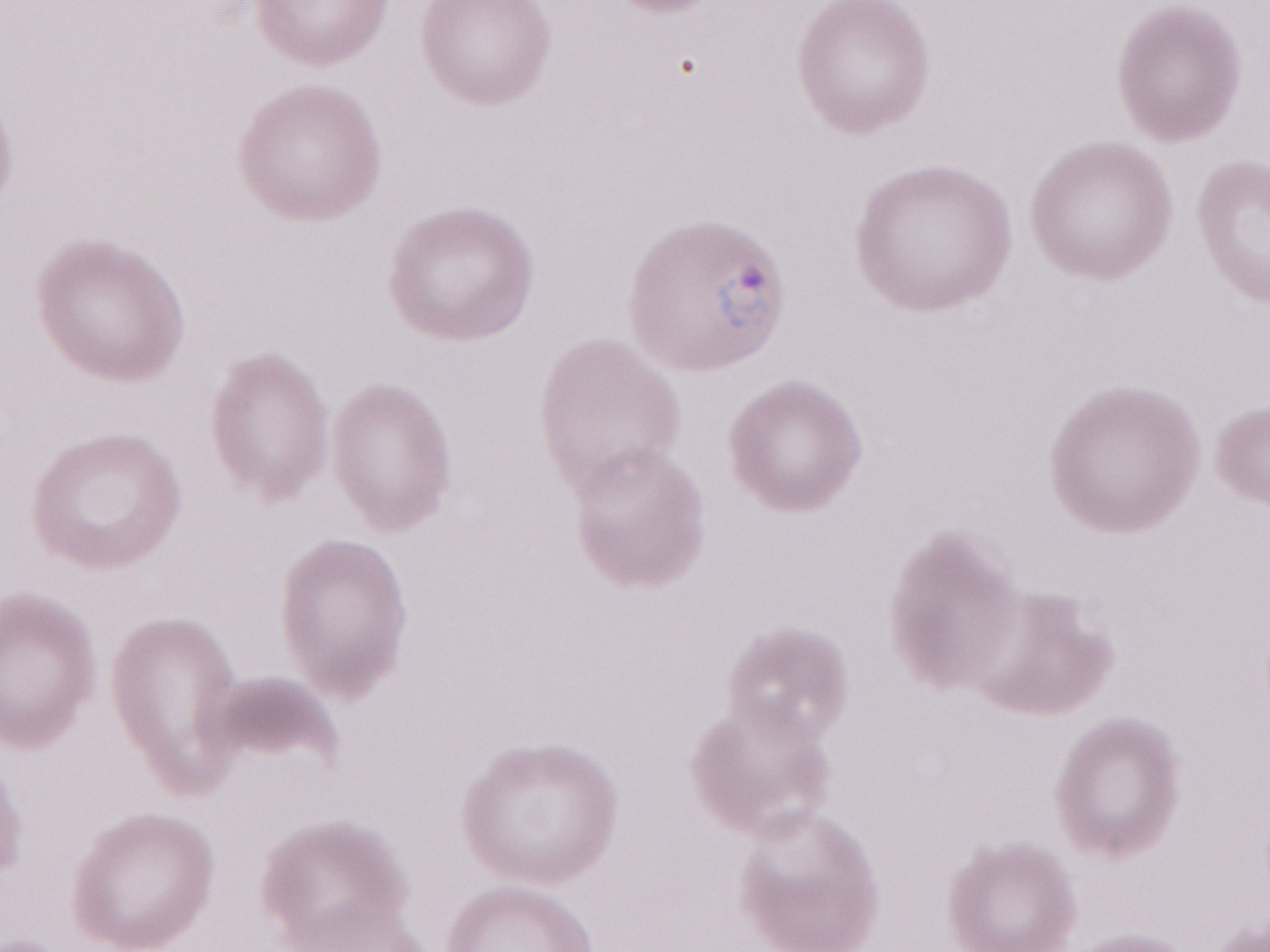
One field of this slide. Patient diagnosis: malaria infection. Image is 1270×952 pixels. May-Grünwald-Giemsa stain. Thin blood smear. Magnification: 1,000x. Olympus BX43 microscope, Olympus DP73 camera.